Outline each uninfected red blood cell.
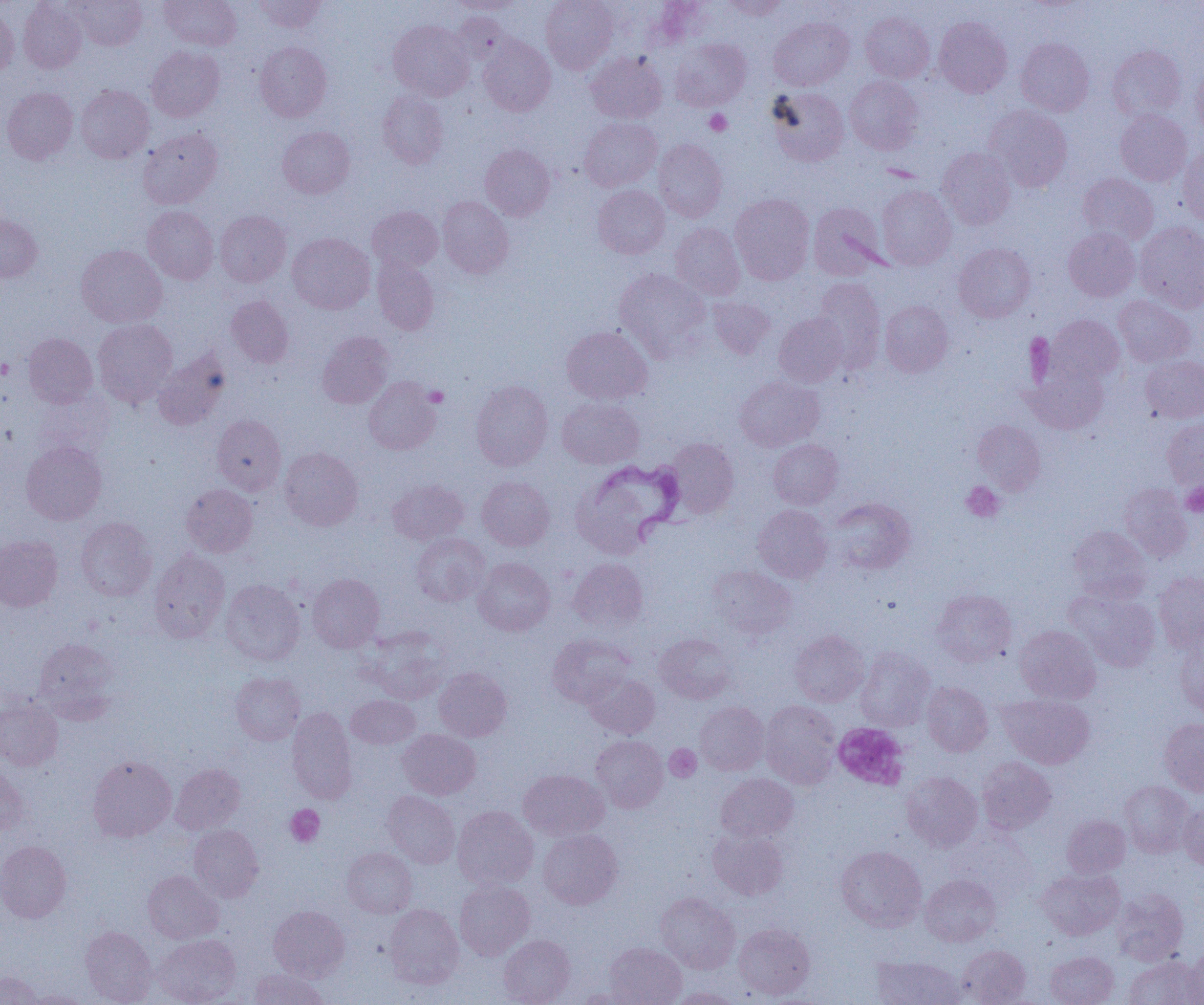
Approximate bounding boxes as (x1, y1, x2, y2) in pixels.
Uninfected red blood cells: (69, 0, 147, 50), (160, 0, 241, 50), (254, 0, 326, 33), (446, 0, 527, 14), (541, 0, 619, 73), (720, 0, 788, 19), (18, 1, 87, 73), (0, 6, 19, 78), (860, 11, 935, 82), (453, 12, 510, 64), (934, 16, 1012, 97), (768, 17, 854, 90), (388, 20, 475, 100), (479, 35, 556, 116), (1016, 37, 1093, 116), (670, 38, 751, 111), (255, 41, 332, 121), (1107, 45, 1186, 121), (146, 46, 224, 121), (586, 52, 667, 123), (1192, 67, 1204, 138), (845, 75, 924, 155), (75, 85, 154, 163), (2, 87, 78, 164), (767, 87, 849, 166), (378, 90, 449, 168), (984, 105, 1073, 191), (1115, 109, 1192, 186), (579, 117, 662, 191), (278, 126, 355, 198), (137, 127, 223, 209), (654, 139, 727, 222), (480, 144, 555, 220), (937, 147, 1016, 230), (1179, 148, 1204, 227), (1078, 173, 1159, 246), (593, 185, 670, 259), (877, 185, 956, 270), (730, 194, 815, 285), (438, 196, 513, 277), (808, 202, 887, 279), (143, 206, 218, 284), (367, 206, 443, 272), (215, 210, 291, 286), (0, 211, 42, 282), (1134, 221, 1204, 312), (671, 223, 745, 300), (1063, 228, 1140, 301), (287, 232, 375, 314), (954, 243, 1035, 322), (76, 244, 166, 328), (372, 255, 439, 335), (614, 268, 711, 360), (812, 278, 885, 372), (226, 295, 294, 368), (1114, 295, 1195, 368), (707, 297, 775, 359), (879, 300, 953, 377), (774, 313, 848, 387), (1048, 315, 1124, 385), (93, 318, 178, 407), (562, 326, 652, 404), (317, 332, 393, 408), (24, 333, 97, 408), (153, 349, 230, 429), (1141, 355, 1204, 423), (1025, 360, 1109, 434), (735, 375, 824, 451), (363, 376, 441, 454), (471, 381, 553, 470), (557, 397, 644, 469), (212, 414, 286, 495), (1162, 417, 1204, 490), (972, 420, 1046, 495), (667, 438, 738, 518), (768, 439, 843, 509), (21, 441, 107, 525), (279, 447, 362, 530), (572, 472, 659, 559), (477, 476, 554, 550), (388, 479, 469, 545), (182, 484, 257, 556), (1119, 484, 1193, 562), (827, 497, 915, 575), (752, 504, 832, 583), (76, 517, 157, 601), (1068, 526, 1151, 602), (411, 533, 490, 606), (0, 534, 62, 611), (149, 549, 229, 642), (473, 557, 554, 636), (568, 557, 648, 632), (706, 564, 797, 641), (1154, 571, 1204, 652), (307, 574, 384, 652), (220, 580, 305, 666), (1066, 588, 1160, 672), (932, 589, 1016, 667), (1015, 625, 1101, 704), (365, 629, 450, 704), (789, 629, 870, 707), (548, 633, 634, 707), (654, 633, 737, 703), (34, 637, 120, 721), (1174, 641, 1204, 715), (855, 648, 935, 731), (434, 667, 512, 741), (231, 672, 304, 745), (582, 672, 660, 738), (921, 682, 993, 756), (347, 694, 420, 748), (999, 694, 1095, 768), (0, 696, 63, 770), (760, 700, 840, 789), (695, 701, 769, 775), (287, 707, 357, 804), (1159, 718, 1204, 796), (398, 729, 481, 799), (591, 735, 668, 812), (87, 755, 177, 841), (976, 757, 1057, 835), (0, 761, 30, 836), (170, 763, 245, 834), (518, 769, 609, 841), (901, 772, 982, 851), (715, 773, 798, 842), (1119, 781, 1194, 857), (382, 791, 460, 868), (1179, 802, 1204, 870), (453, 805, 538, 890), (1062, 815, 1131, 878), (189, 825, 263, 902), (707, 827, 789, 900), (538, 829, 622, 909), (0, 841, 71, 922), (836, 845, 927, 931), (342, 847, 417, 918), (1036, 868, 1124, 940), (143, 870, 223, 944), (920, 874, 1001, 947), (455, 880, 534, 959), (1112, 888, 1188, 965), (655, 892, 740, 973), (384, 904, 463, 989), (268, 905, 349, 981), (733, 923, 814, 999), (80, 926, 157, 1005), (153, 934, 241, 1004), (499, 935, 575, 1005), (605, 942, 687, 1004), (957, 945, 1031, 1004), (1183, 945, 1204, 1005), (1045, 951, 1118, 1005), (871, 956, 965, 1005), (1123, 956, 1202, 1005), (249, 968, 327, 1004), (0, 971, 43, 1005), (571, 987, 647, 1004), (667, 988, 743, 1005), (25, 991, 93, 1004).

Summary:
  - Platelet locations: (704, 109, 732, 136), (0, 359, 13, 379), (424, 386, 448, 407), (1180, 481, 1204, 517), (960, 482, 1005, 522), (833, 722, 909, 790), (665, 744, 701, 782), (285, 804, 324, 847)
  - Trypanosoma brucei locations: (592, 458, 690, 546)
  - Slide-level diagnosis: Trypanosoma brucei
  - Image size: 1204×1005 pixels
  - Preparation: thin blood smear
  - Magnification: 1000x
  - Field of view: one of a larger specimen
  - Modality: optical microscopy